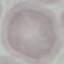

result = negative for malaria parasites
image type = cell patch, automatically extracted from a larger field of view and resized to 64 × 64 pixels
capture = smartphone camera at the microscope eyepiece
preparation = thin blood film
stain = Giemsa